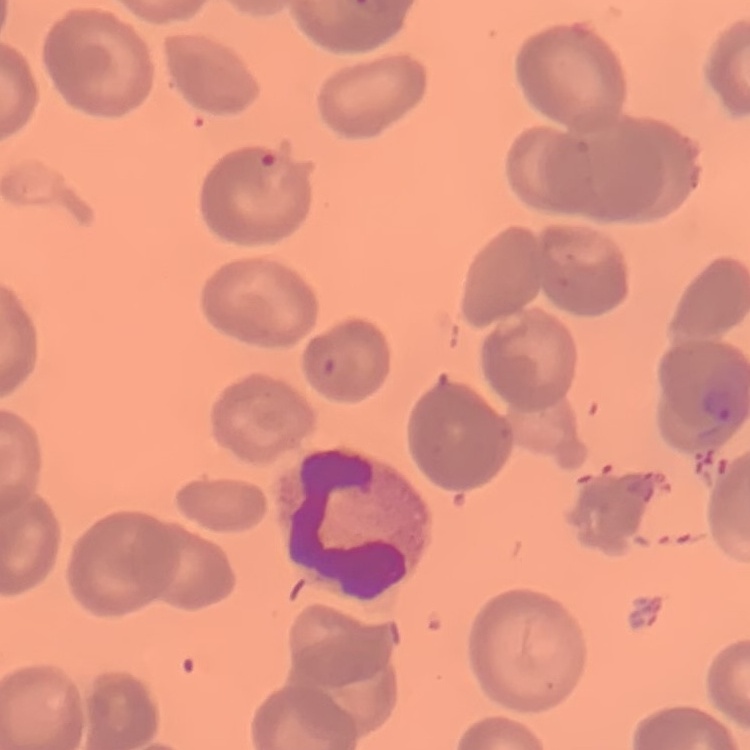

The erythrocytes exhibit no rouleaux formation. Field's or Giemsa stain. Square crop of a larger photomicrograph. Thin blood smear.